Locate every Plasmodium parasite.
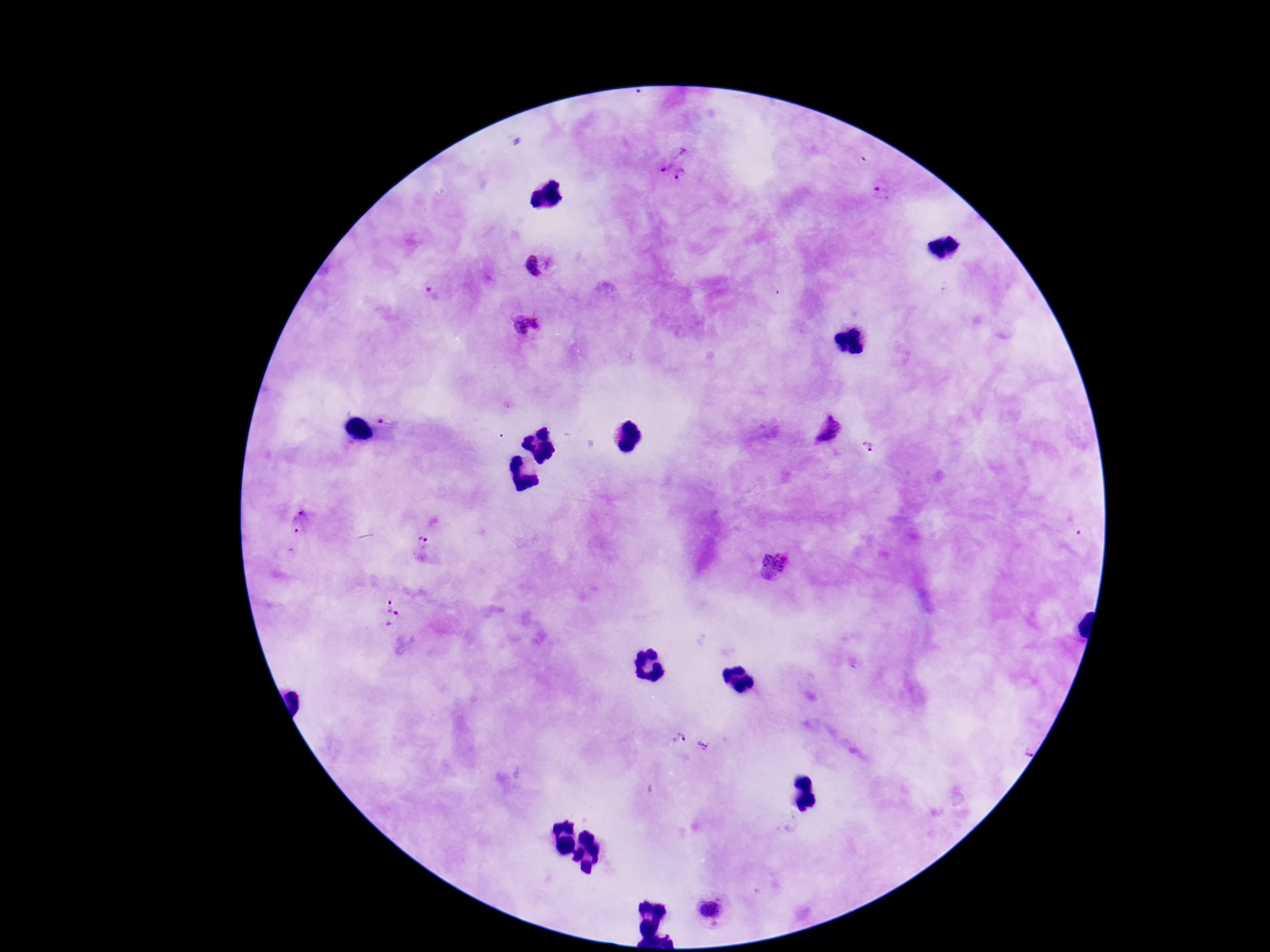

Approximate centers as [x, y] in pixels.
Plasmodium parasites: [666, 153], [683, 175], [882, 193], [534, 265], [527, 324], [388, 421], [828, 430], [868, 445], [297, 523], [422, 541], [773, 565], [386, 603], [396, 620], [679, 739], [702, 746], [711, 911].

field_of_view: single
preparation: thick blood film
image_size: 1270×952 pixels
magnification: 100x
capture: smartphone camera through the microscope eyepiece
stain: Giemsa
patient_malaria_status: infected